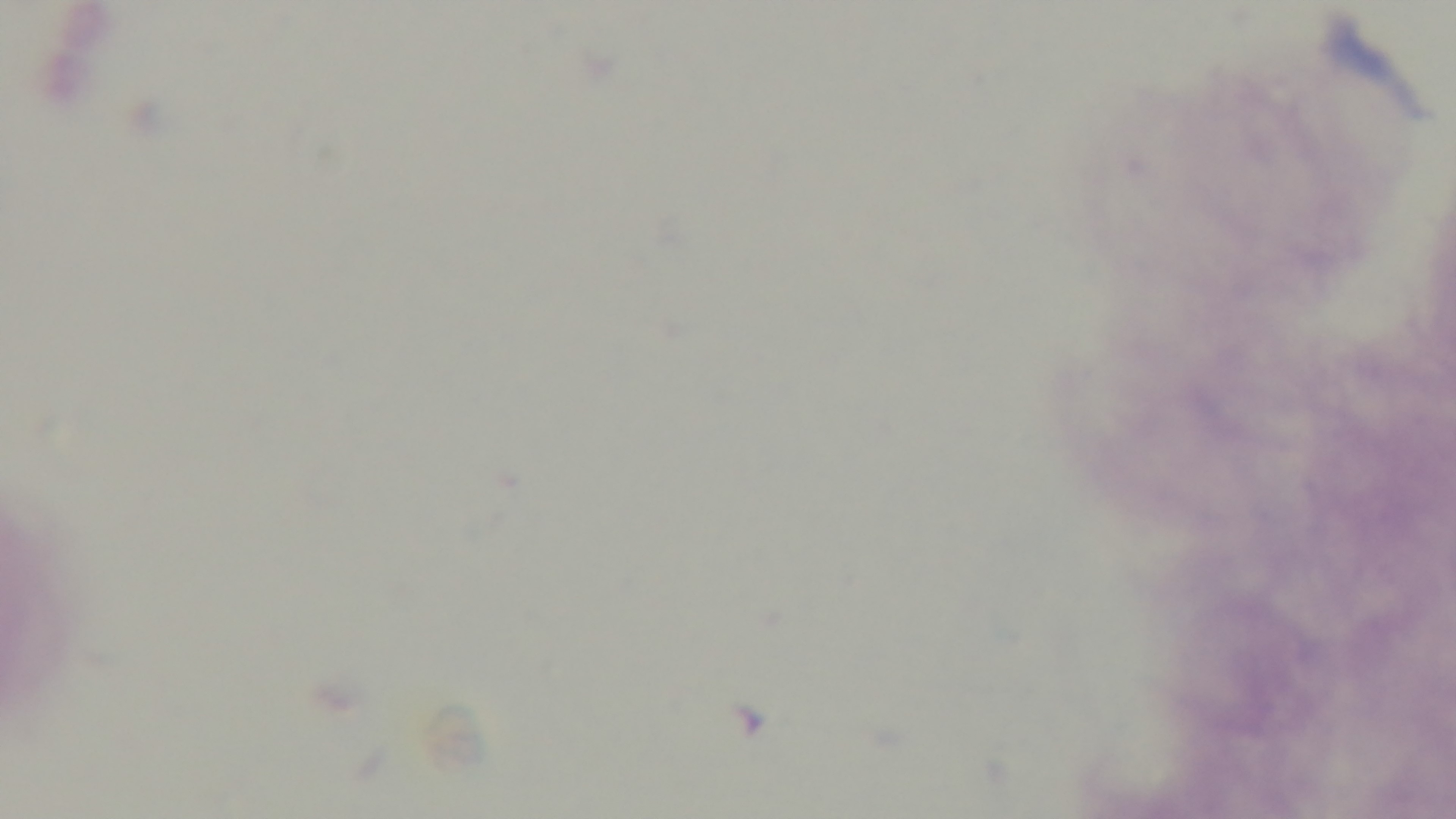
Summary:
  - Capture: mounted 4K digital camera
  - Malaria status: uninfected
  - Modality: light microscopy
  - Stain: Giemsa
  - Field of view: single
  - Objective: 100x oil immersion
  - Preparation: thick blood film